Name the blood parasite species.
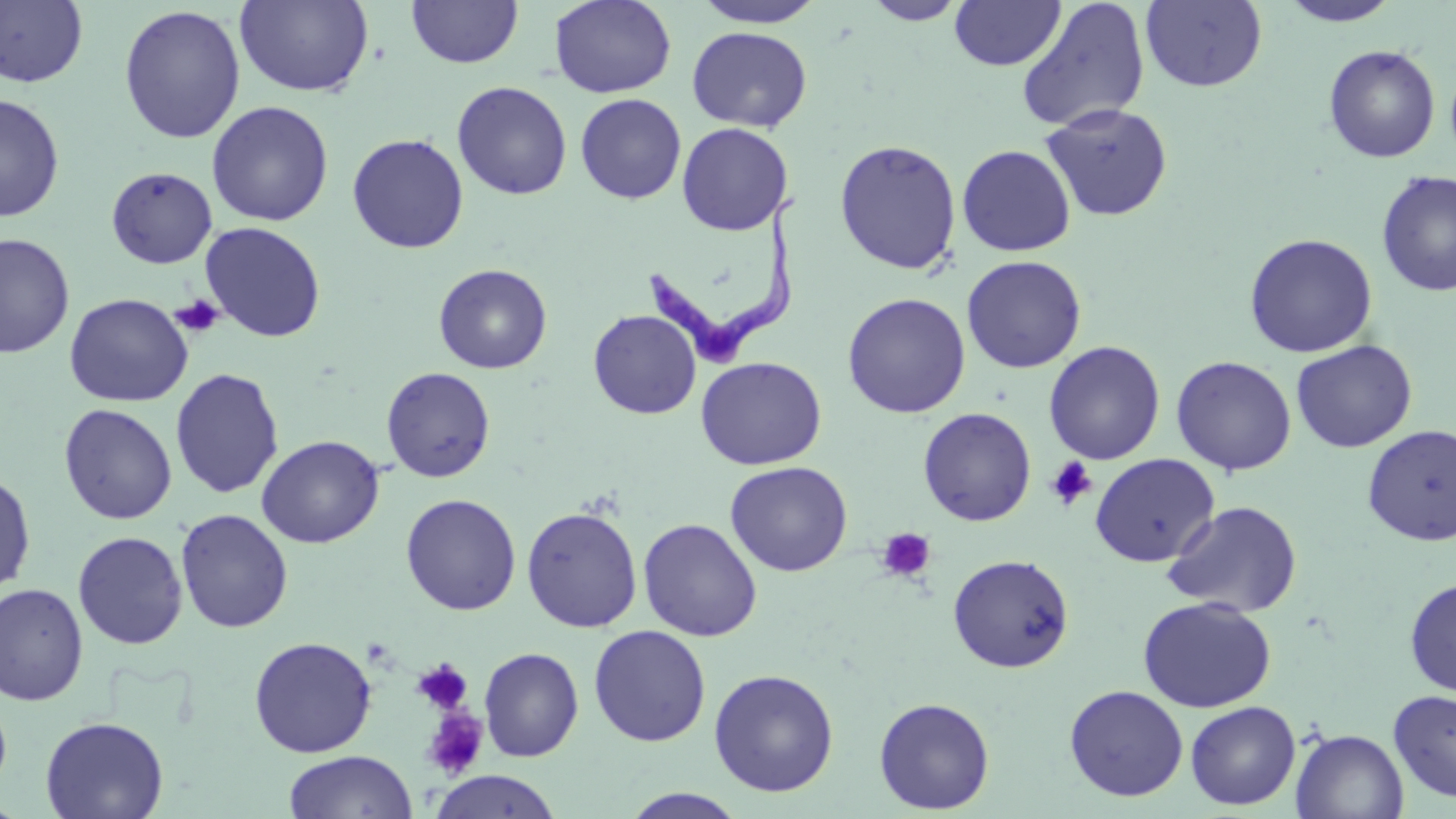
Trypanosoma brucei.

modality: light microscopy
preparation: thin blood film
magnification: 1000x
trypanosoma_brucei_locations: 'approximate bounding boxes as [x1, y1, x2, y2] in pixels: [647, 196, 801, 367]'
uninfected_red_blood_cell_locations: 'approximate bounding boxes as [x1, y1, x2, y2] in pixels: [236, 0, 374, 98], [548, 0, 677, 98], [691, 0, 828, 28], [1016, 0, 1151, 133], [1141, 0, 1267, 92], [0, 1, 89, 88], [406, 1, 523, 68], [862, 1, 969, 25], [949, 1, 1065, 71], [1279, 1, 1402, 27], [118, 5, 246, 144], [686, 26, 812, 131], [1323, 44, 1440, 163], [451, 81, 572, 200], [575, 93, 687, 204], [0, 94, 65, 223], [206, 100, 333, 227], [1040, 102, 1173, 221], [676, 122, 793, 235], [346, 133, 469, 254], [834, 139, 962, 275], [956, 144, 1076, 256], [106, 166, 217, 268], [1376, 169, 1456, 297], [200, 222, 326, 342], [1243, 232, 1379, 358], [1, 233, 74, 359], [961, 255, 1087, 374], [434, 263, 552, 374], [64, 293, 193, 407], [842, 293, 971, 419], [588, 309, 701, 420], [1291, 339, 1418, 453], [1044, 340, 1165, 465], [1170, 355, 1297, 475], [695, 356, 827, 470], [381, 366, 496, 483], [170, 367, 284, 498], [59, 404, 177, 524], [917, 407, 1037, 526], [1361, 425, 1456, 545], [256, 435, 384, 548], [1090, 453, 1219, 567], [725, 461, 852, 577], [0, 470, 36, 597], [400, 494, 521, 615], [1162, 500, 1304, 617], [521, 506, 643, 633], [175, 508, 293, 633], [638, 517, 762, 641], [72, 531, 188, 649], [947, 553, 1075, 673], [1404, 578, 1456, 698], [0, 582, 88, 706], [1137, 596, 1277, 712], [588, 625, 711, 747], [248, 636, 377, 757], [478, 646, 584, 762], [708, 668, 839, 797], [1063, 684, 1189, 801], [1388, 689, 1456, 804], [873, 697, 995, 814], [1185, 701, 1301, 810], [40, 715, 169, 819], [1291, 728, 1409, 818], [283, 750, 417, 818], [428, 770, 563, 818], [619, 788, 748, 819]'
stain: May-Grünwald-Giemsa
image_size: 1456×819 pixels
platelet_locations: 'approximate bounding boxes as [x1, y1, x2, y2] in pixels: [171, 295, 225, 338], [1045, 456, 1098, 511], [875, 527, 936, 583], [411, 658, 474, 716], [421, 707, 490, 781]'
field_of_view: one of a larger specimen